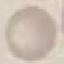
result: no malaria parasites seen
stain: Giemsa
capture: smartphone camera at the microscope eyepiece
image_type: automatically extracted cell patch, resized to 64 × 64 pixels
preparation: thin smear